State the preparation type.
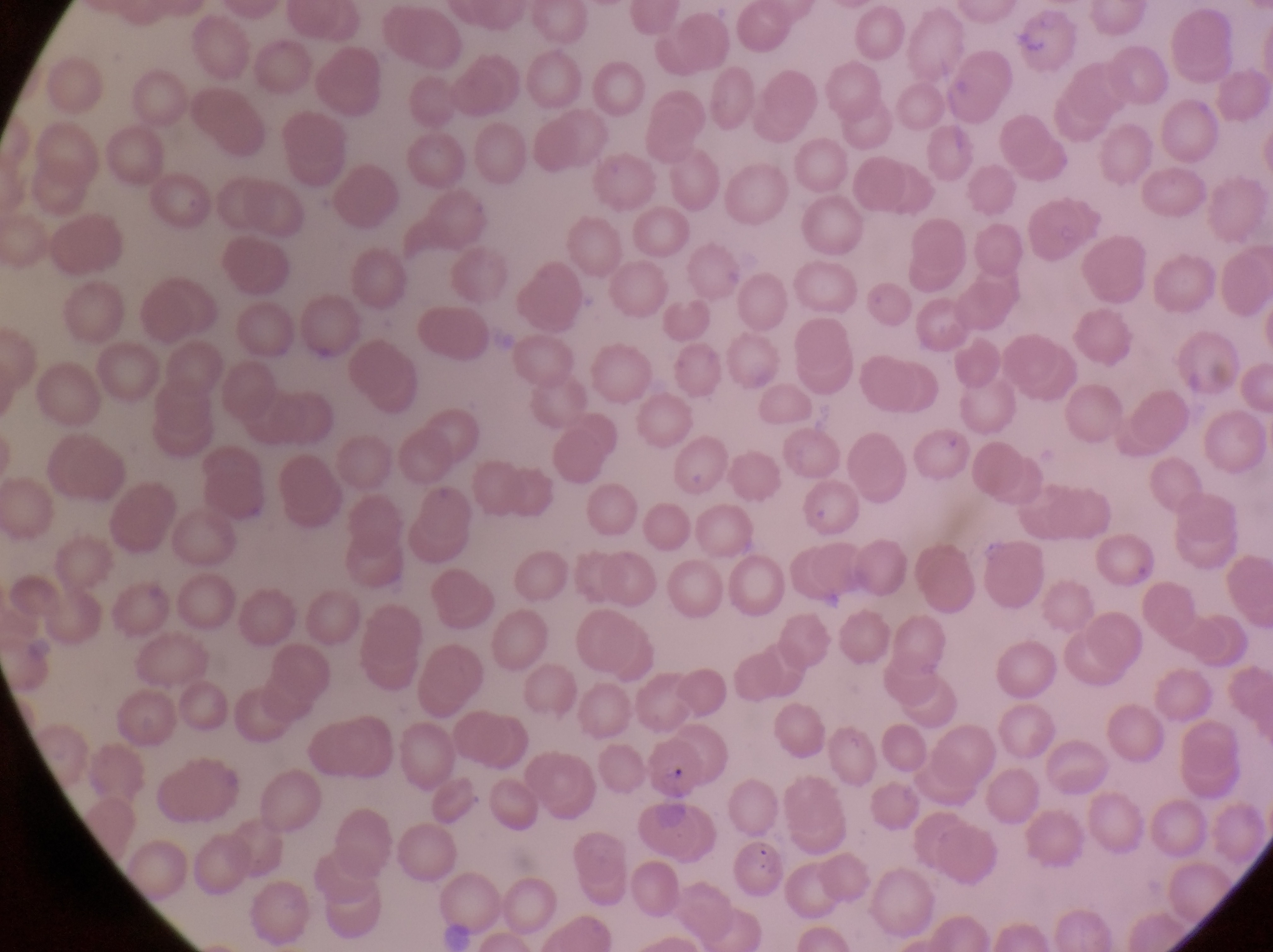

Thin blood film.

{
  "capture": "smartphone photograph through the eyepiece of an Olympus CX-23 microscope",
  "image_size": "1273×952 pixels",
  "parasitised_red_blood_cell_locations": "approximate bounding boxes as (left, top, right, bottom) in pixels: (646, 739, 704, 796), (735, 835, 786, 888)",
  "country": "Uganda",
  "field_of_view": "single",
  "magnification": "1000x"
}